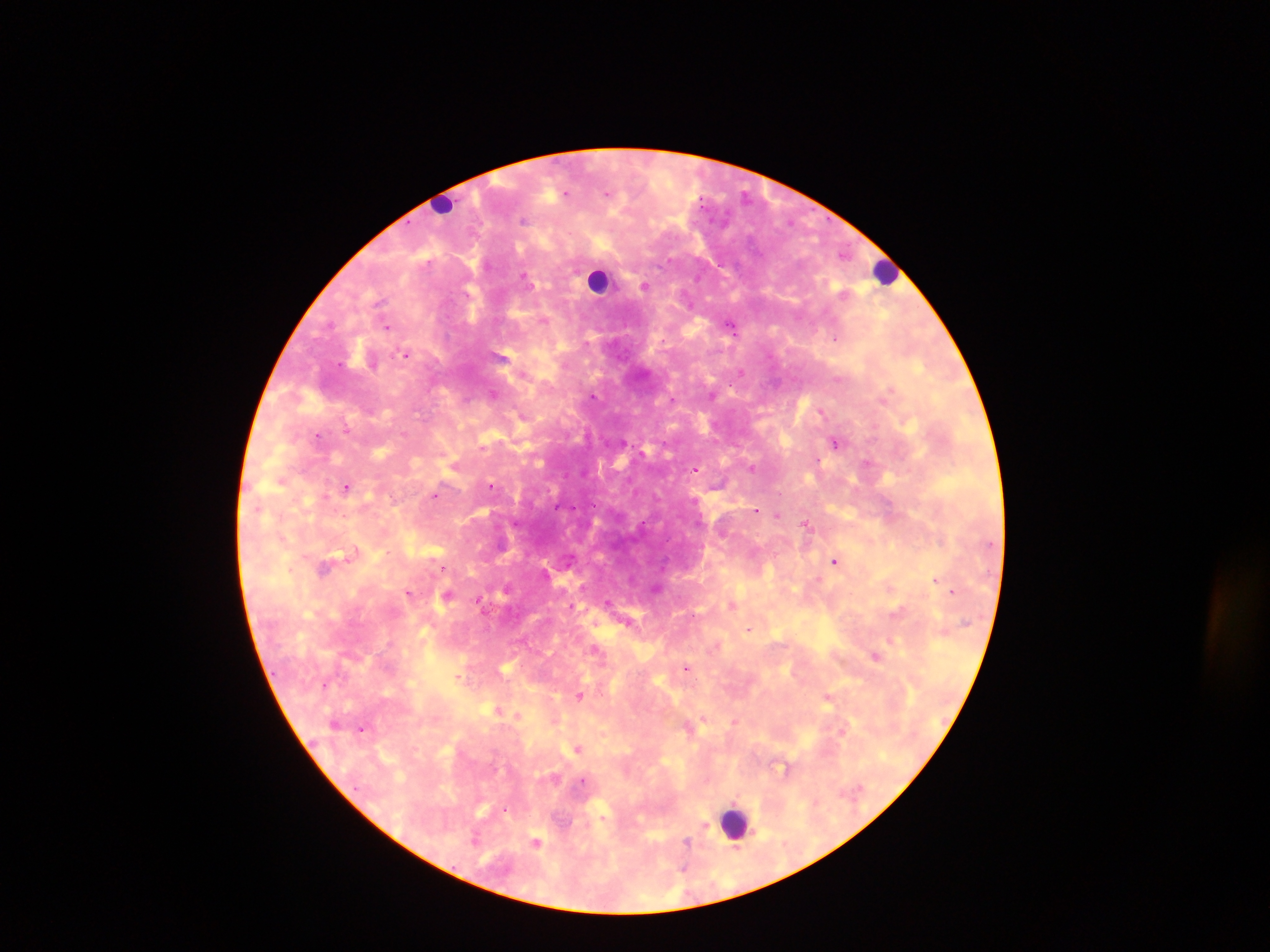
Approximate centers as (x, y) in pixels.
Summary:
  - Leukocyte locations: (441, 203), (884, 272), (599, 280), (734, 822)
  - Malaria parasite locations: (606, 193), (565, 195), (524, 221), (844, 252), (524, 276), (645, 285), (379, 302), (330, 323), (730, 326), (387, 327), (835, 339), (406, 354), (740, 372), (523, 373), (493, 393), (593, 396), (673, 399), (822, 411), (346, 429), (318, 436), (623, 442), (834, 442), (817, 460), (866, 463), (752, 467), (695, 470), (492, 485), (347, 487), (435, 495), (756, 509), (777, 515), (698, 522), (806, 524), (353, 552), (835, 560), (325, 567), (443, 568), (936, 579), (952, 591), (408, 593), (446, 596), (478, 601), (608, 602), (570, 606), (748, 629), (596, 650), (875, 656), (686, 667), (580, 695), (828, 697), (735, 721), (362, 728), (842, 732), (578, 748), (703, 825), (474, 840), (536, 842), (687, 843), (685, 869)
  - Capture: mobile-phone photograph through a microscope
  - Image size: 1270×952 pixels
  - Field of view: single
  - Preparation: thick blood smear
  - Country: Ghana